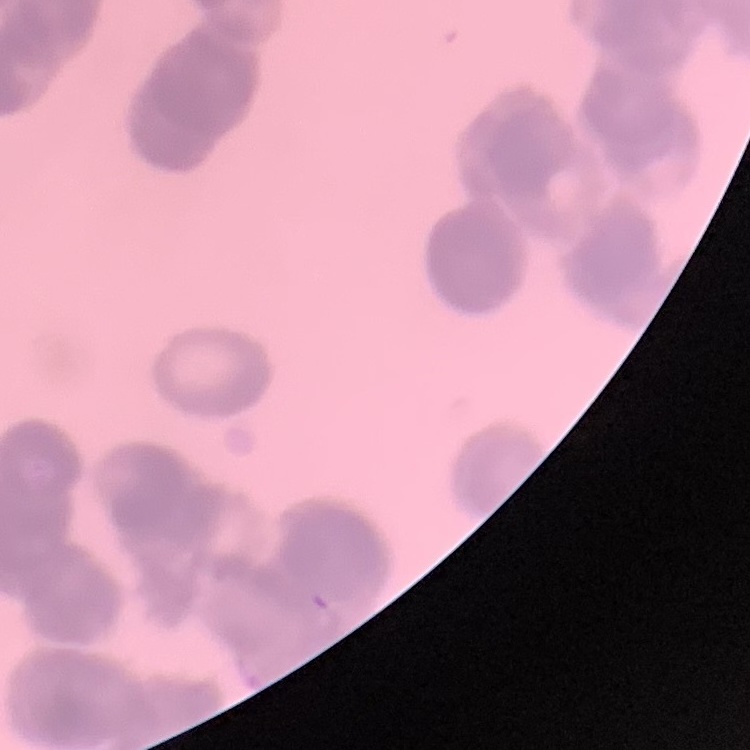
erythrocyte morphology = rouleaux formation
stain = Field's or Giemsa
image type = one tile cut from a larger photomicrograph
preparation = thin peripheral smear